Name the parasite shown.
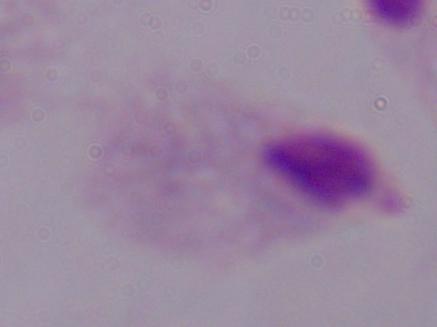
A trichomonad.

modality: photomicrograph
magnification: 1000x